Assess the morphology of the red blood cells.
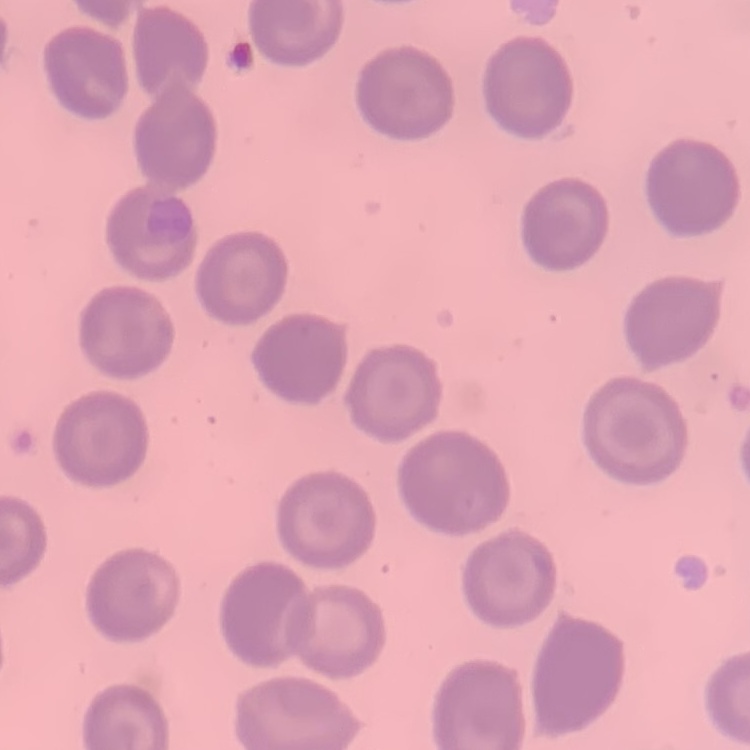

They show no rouleaux formation.

preparation = thin blood film
stain = Field's or Giemsa
image type = square crop of a larger photomicrograph